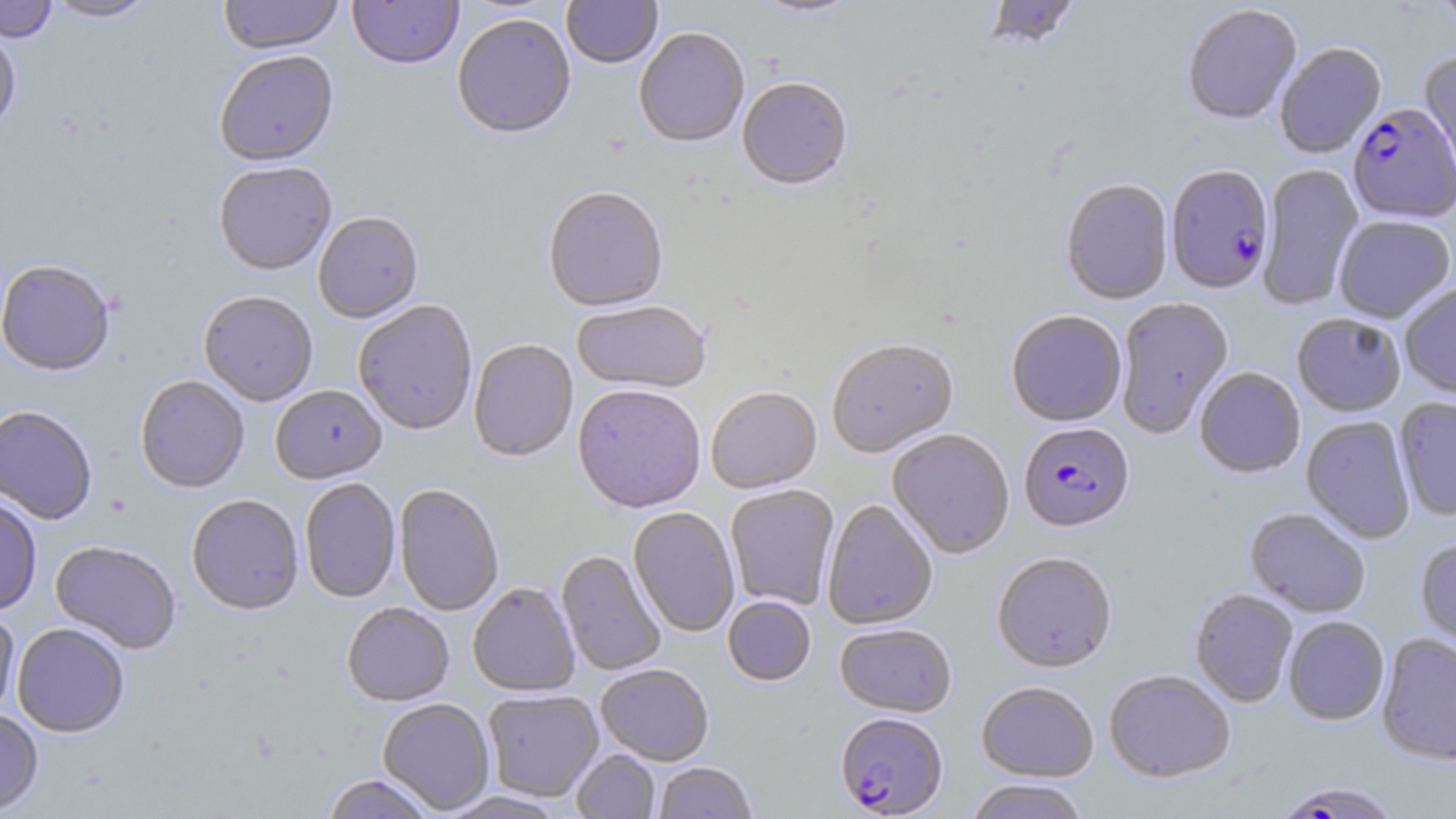
Summary:
  - Coordinate format: approximate bounding boxes as [x1, y1, x2, y2] in pixels
  - Uninfected red blood cell locations: [0, 0, 58, 42], [42, 0, 156, 23], [218, 0, 343, 55], [348, 0, 464, 71], [561, 0, 663, 70], [748, 0, 864, 20], [1434, 0, 1456, 31], [984, 1, 1080, 53], [1182, 6, 1302, 127], [452, 14, 576, 141], [0, 26, 21, 135], [634, 29, 749, 150], [1274, 44, 1387, 160], [1418, 50, 1456, 188], [214, 51, 339, 169], [736, 79, 853, 193], [213, 163, 336, 277], [1257, 164, 1364, 310], [1060, 179, 1174, 306], [542, 188, 668, 313], [313, 213, 423, 325], [1334, 216, 1454, 325], [0, 260, 115, 377], [1399, 284, 1456, 401], [198, 292, 318, 406], [1115, 299, 1234, 439], [352, 301, 477, 436], [572, 302, 711, 396], [1006, 312, 1127, 428], [1292, 315, 1406, 418], [469, 341, 578, 463], [827, 341, 959, 459], [1194, 368, 1305, 480], [135, 376, 250, 493], [270, 385, 387, 485], [572, 386, 706, 515], [706, 389, 822, 496], [1395, 397, 1456, 521], [0, 405, 98, 524], [1300, 416, 1415, 544], [887, 430, 1014, 561], [299, 478, 400, 603], [393, 485, 504, 617], [725, 486, 840, 610], [0, 494, 42, 616], [187, 495, 304, 615], [822, 500, 938, 632], [627, 508, 740, 638], [1245, 508, 1371, 618], [1414, 537, 1456, 659], [50, 541, 181, 654], [556, 551, 666, 676], [992, 554, 1117, 674], [468, 583, 580, 697], [1189, 589, 1298, 708], [722, 597, 816, 687], [342, 603, 454, 707], [0, 610, 20, 720], [1283, 617, 1389, 726], [12, 622, 129, 738], [835, 624, 957, 718], [1376, 634, 1456, 766], [596, 665, 714, 766], [1104, 671, 1236, 784], [976, 683, 1098, 782], [483, 690, 603, 802], [377, 699, 495, 814], [0, 710, 43, 816], [572, 750, 660, 819], [653, 762, 757, 819], [322, 774, 436, 819], [965, 780, 1090, 819], [439, 791, 570, 818]
  - Plasmodium falciparum-infected red blood cell locations: [1347, 105, 1455, 225], [1165, 167, 1275, 296], [1019, 424, 1134, 534], [835, 714, 948, 817], [1273, 782, 1404, 818]
  - Slide-level diagnosis: Plasmodium falciparum
  - Field of view: single
  - Preparation: thin blood smear
  - Stain: May-Grünwald-Giemsa
  - Magnification: 1000x
  - Image size: 1456×819 pixels
  - Modality: light microscopy